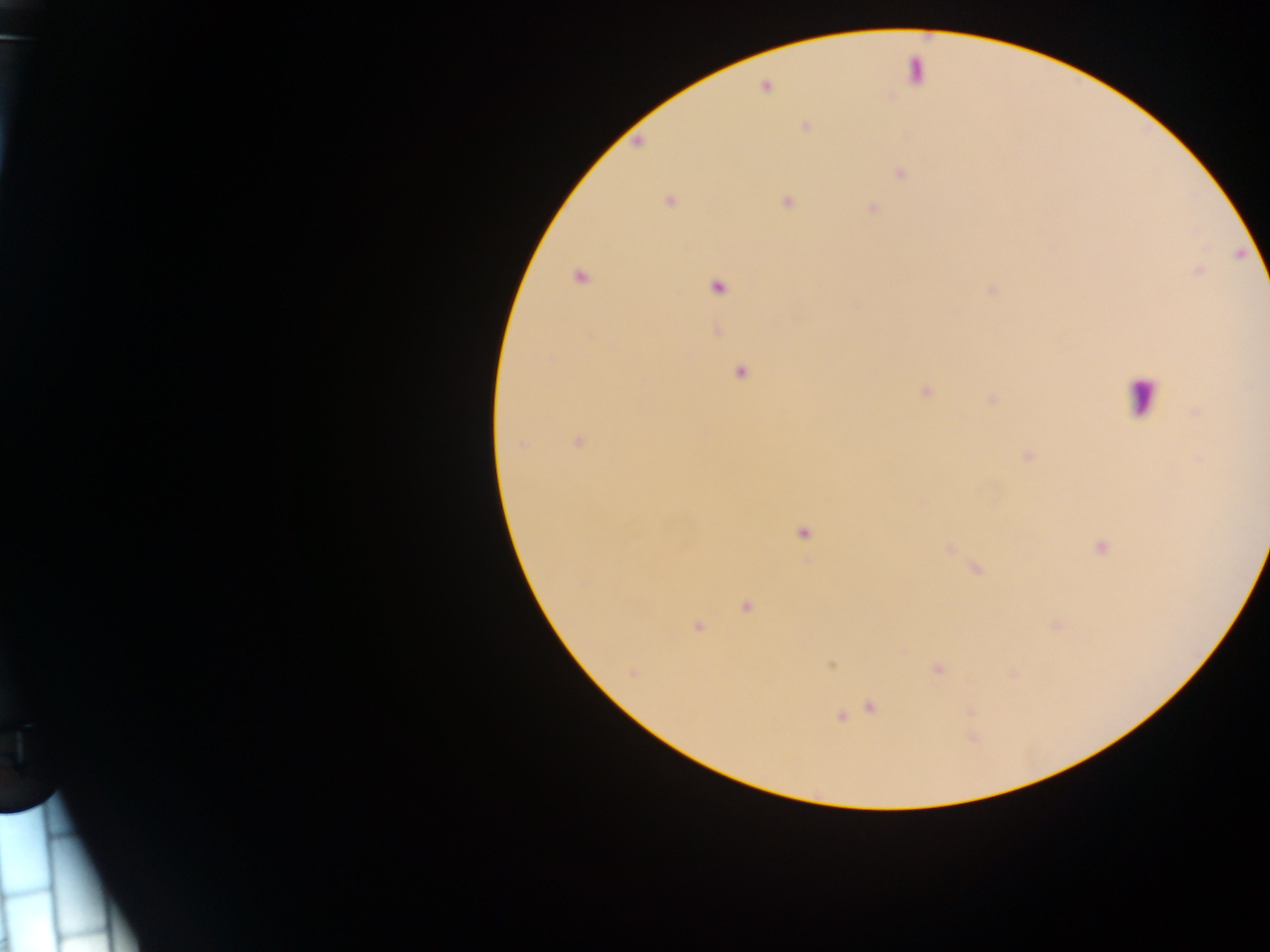

Approximate centers as [x, y] in pixels. Malaria parasite locations: [765, 87], [805, 127], [901, 174], [670, 201], [787, 202], [872, 208], [579, 278], [717, 288], [591, 335], [741, 372], [926, 391], [992, 399], [1196, 412], [579, 442], [521, 444], [1026, 456], [804, 533], [949, 548], [1100, 548], [977, 570], [746, 607], [1057, 626], [697, 627], [832, 665], [937, 669], [632, 673], [871, 706], [841, 716]. Leukocyte locations: [1142, 396]. Thick blood smear. One field of view. Collected in Ghana. Photographed through a microscope with a mobile-phone camera. Image is 1270×952 pixels.